Classify this cell by malaria status.
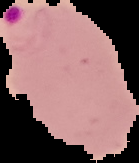

Parasitized.

image size = 139×163 pixels
preparation = thin blood smear
image type = cell region segmented out of the field of view; surrounding area masked to black